State which parasite is depicted.
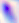
Toxoplasma gondii.

modality = photomicrograph
magnification = 400x